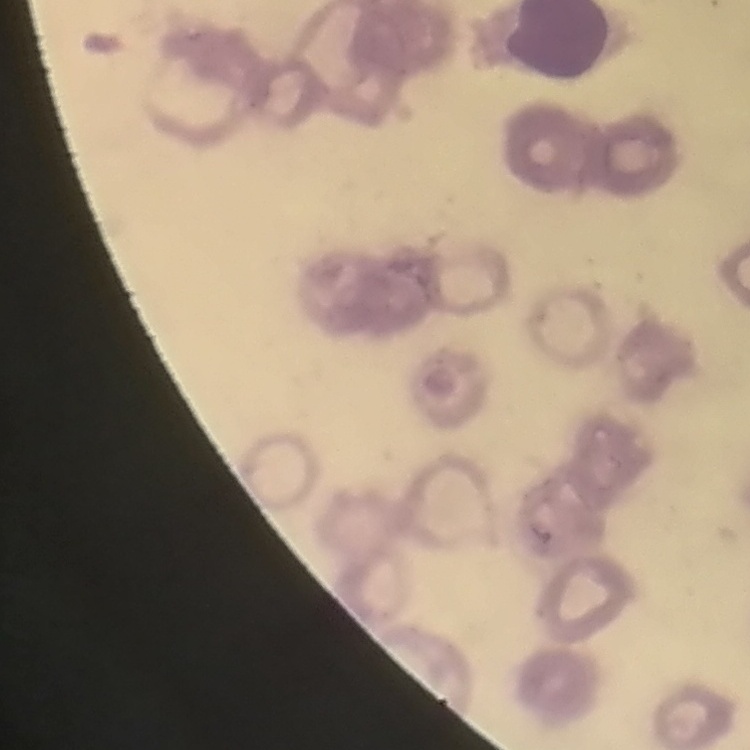

The erythrocytes show rouleaux formation. Thin blood film. Field's or Giemsa stain. One tile cut from a larger photomicrograph.